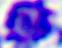

A white blood cell is seen. Micrograph. Captured at 400x magnification.